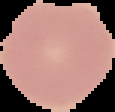

Summary:
  - Preparation: thin blood smear
  - Result: negative for malaria parasites
  - Image size: 115×112 pixels
  - Image type: cell region segmented out of the field of view; surrounding area masked to black